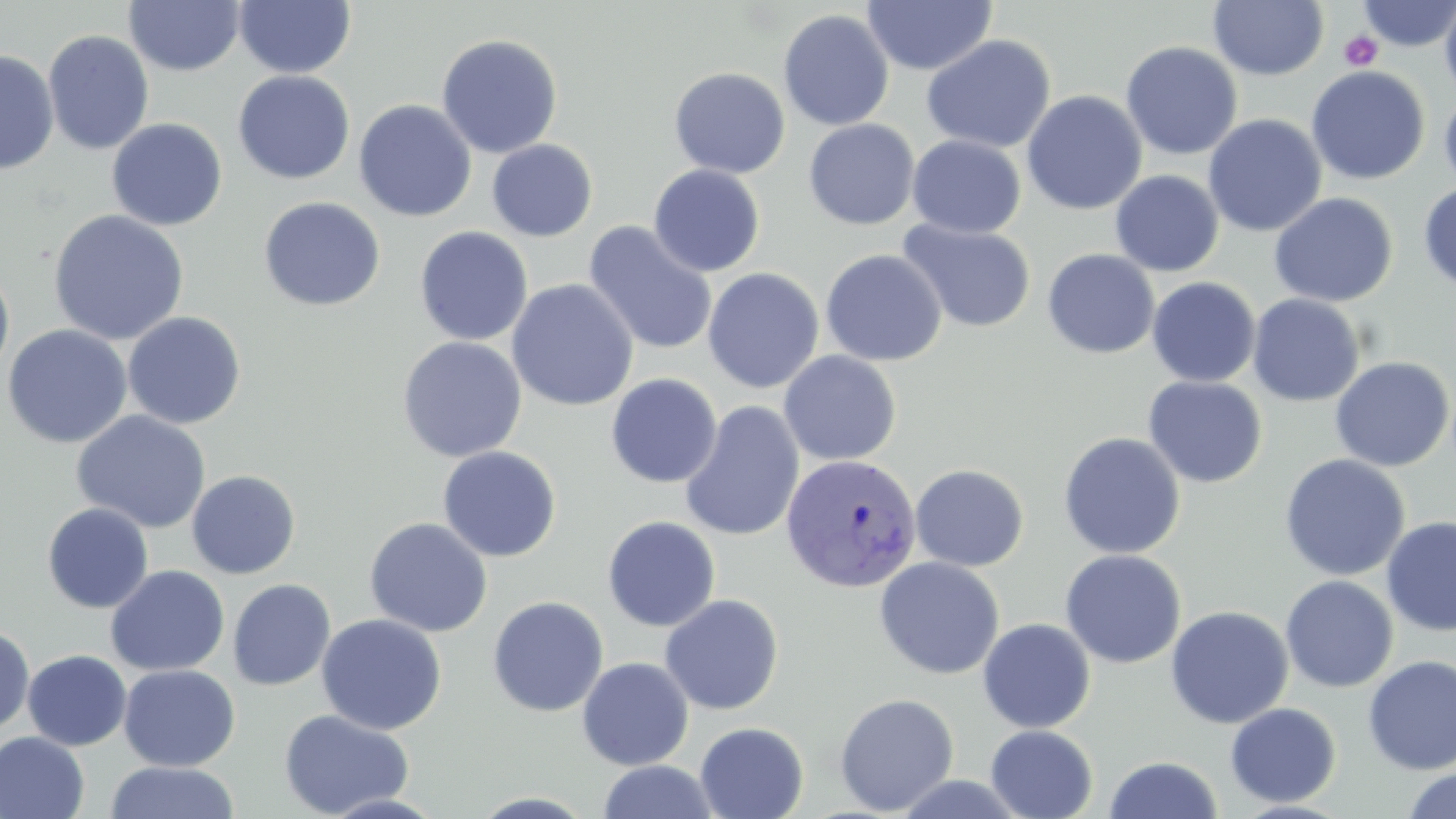
Summary:
  - Coordinate format: approximate bounding boxes as (x1, y1, x2, y2) in pixels
  - Plasmodium vivax-infected red blood cell locations: (780, 454, 922, 593)
  - Platelet locations: (1339, 30, 1383, 71)
  - Uninfected red blood cell locations: (234, 0, 357, 79), (1357, 0, 1456, 51), (1439, 0, 1456, 105), (124, 1, 245, 76), (862, 1, 997, 75), (1208, 1, 1329, 81), (777, 9, 894, 131), (42, 30, 154, 155), (436, 33, 563, 159), (921, 35, 1057, 154), (1120, 41, 1243, 160), (0, 49, 59, 175), (1306, 66, 1430, 185), (668, 67, 790, 179), (233, 70, 356, 184), (1439, 88, 1456, 197), (1022, 90, 1147, 215), (354, 99, 477, 222), (1203, 114, 1327, 237), (106, 118, 227, 231), (803, 119, 919, 230), (907, 135, 1026, 237), (487, 139, 598, 241), (648, 165, 766, 277), (1110, 170, 1224, 277), (1418, 183, 1456, 292), (1268, 193, 1398, 307), (258, 196, 386, 311), (48, 210, 190, 346), (898, 219, 1037, 334), (582, 221, 718, 356), (414, 226, 533, 346), (1042, 248, 1160, 359), (820, 249, 947, 367), (0, 260, 15, 384), (702, 267, 824, 393), (1147, 276, 1261, 387), (506, 279, 639, 411), (1247, 294, 1365, 407), (122, 311, 246, 429), (2, 324, 133, 449), (397, 336, 527, 463), (778, 350, 902, 466), (1329, 356, 1455, 472), (605, 373, 722, 489), (1142, 375, 1267, 488), (679, 400, 805, 542), (71, 410, 212, 534), (1058, 432, 1186, 559), (437, 446, 562, 562), (1279, 454, 1410, 581), (910, 463, 1029, 571), (186, 470, 301, 579), (41, 502, 154, 614), (601, 515, 721, 632), (1381, 515, 1456, 636), (364, 517, 493, 637), (1059, 549, 1186, 669), (874, 556, 1005, 680), (106, 565, 229, 676), (1280, 575, 1399, 692), (228, 579, 336, 691), (659, 594, 784, 715), (487, 595, 609, 717), (1165, 605, 1294, 728), (316, 613, 447, 735), (977, 618, 1096, 733), (0, 625, 35, 733), (22, 650, 132, 751), (1362, 655, 1456, 775), (576, 657, 694, 771), (119, 664, 240, 771), (834, 693, 960, 815), (1224, 702, 1341, 807), (278, 709, 414, 818), (695, 722, 808, 819), (985, 724, 1098, 819), (0, 732, 89, 819), (1104, 756, 1223, 818), (596, 760, 722, 819), (105, 761, 239, 819), (1400, 766, 1456, 819)
  - Slide-level diagnosis: Plasmodium vivax
  - Field of view: single
  - Modality: optical microscopy
  - Stain: May-Grünwald-Giemsa
  - Image size: 1456×819 pixels
  - Magnification: 1000x
  - Preparation: thin blood smear